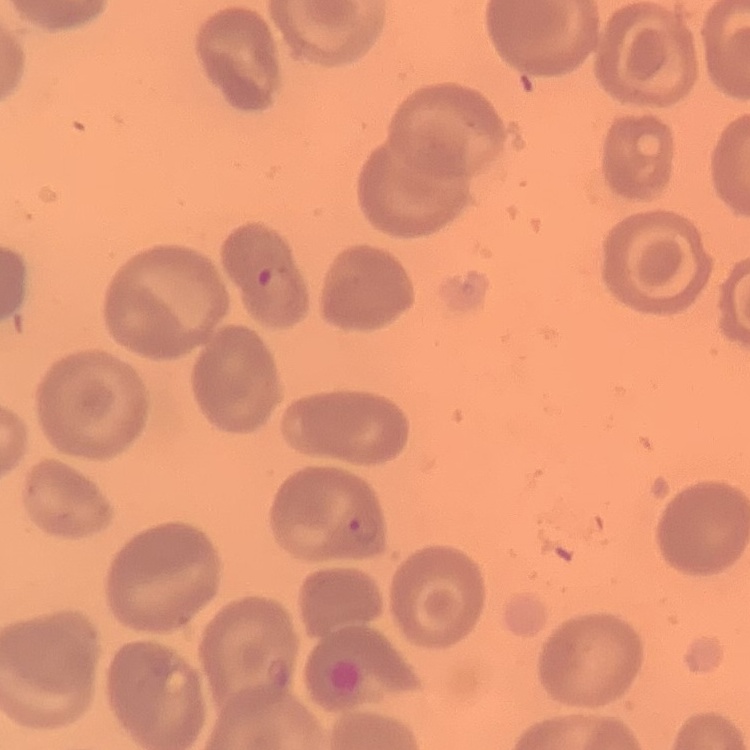

The red blood cells show no rouleaux formation. One tile cut from a larger photomicrograph. Thin blood smear. Stained with either Field's or Giemsa.